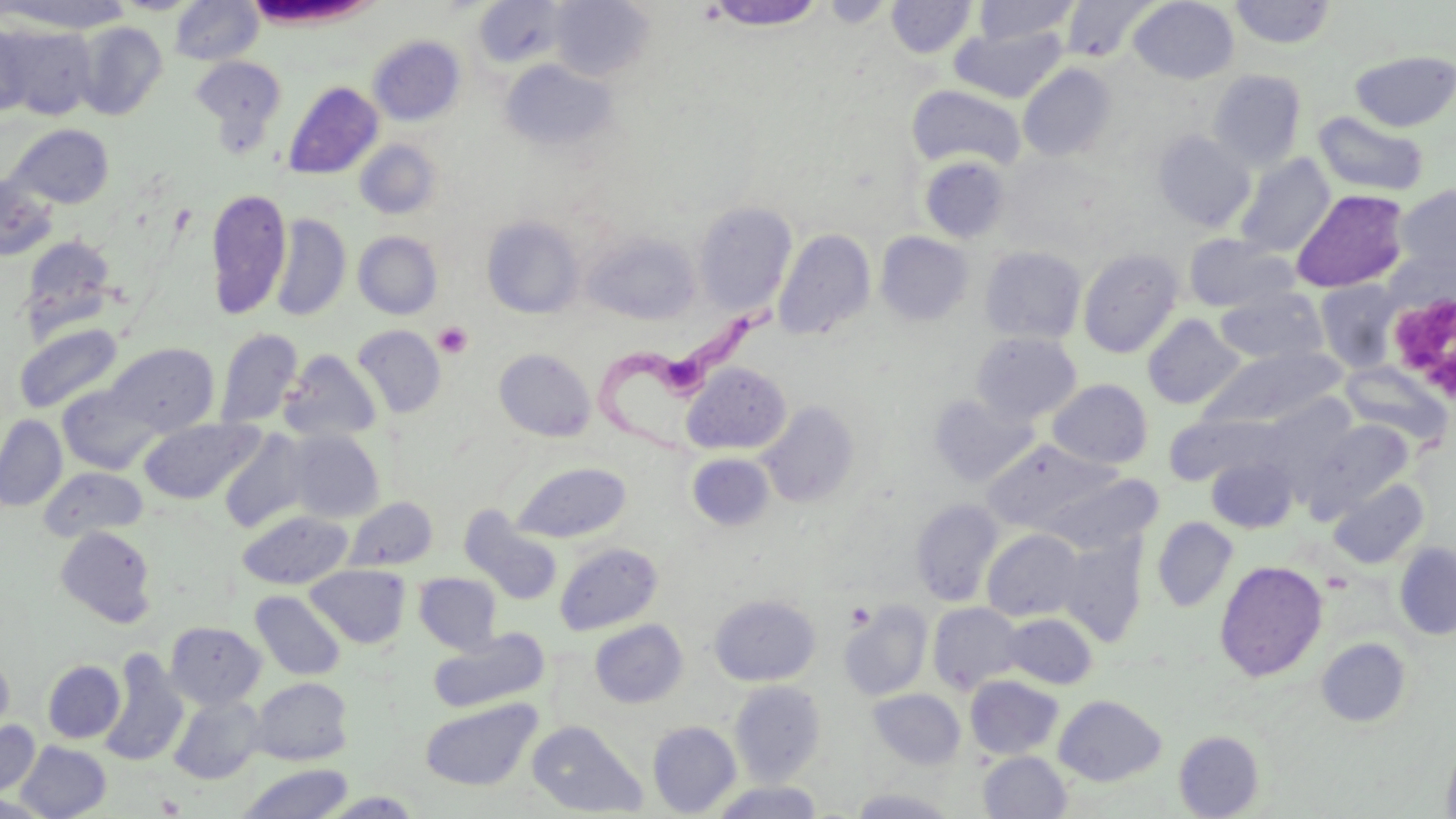

Approximate bounding boxes as named x1/y1/x2/y2 corners in pixels. Platelet locations: (x1=1386, y1=285, x2=1455, y2=409), (x1=434, y1=321, x2=473, y2=359), (x1=156, y1=794, x2=185, y2=816). Trypanosoma brucei locations: (x1=593, y1=297, x2=779, y2=458). Uninfected red blood cell locations: (x1=1, y1=0, x2=133, y2=33), (x1=170, y1=0, x2=263, y2=65), (x1=549, y1=0, x2=655, y2=82), (x1=886, y1=0, x2=977, y2=58), (x1=973, y1=0, x2=1079, y2=45), (x1=1129, y1=0, x2=1239, y2=84), (x1=472, y1=1, x2=568, y2=70), (x1=703, y1=1, x2=828, y2=31), (x1=1059, y1=1, x2=1154, y2=62), (x1=1229, y1=1, x2=1337, y2=49), (x1=73, y1=21, x2=168, y2=121), (x1=0, y1=23, x2=32, y2=117), (x1=2, y1=24, x2=97, y2=120), (x1=951, y1=26, x2=1067, y2=103), (x1=368, y1=36, x2=465, y2=125), (x1=1350, y1=50, x2=1456, y2=132), (x1=191, y1=56, x2=285, y2=140), (x1=500, y1=59, x2=617, y2=152), (x1=1018, y1=63, x2=1118, y2=162), (x1=1207, y1=69, x2=1306, y2=170), (x1=282, y1=81, x2=383, y2=180), (x1=907, y1=85, x2=1025, y2=171), (x1=1312, y1=111, x2=1429, y2=197), (x1=7, y1=123, x2=114, y2=209), (x1=1154, y1=130, x2=1255, y2=232), (x1=354, y1=139, x2=442, y2=219), (x1=1235, y1=153, x2=1334, y2=257), (x1=919, y1=155, x2=1011, y2=243), (x1=0, y1=173, x2=59, y2=263), (x1=1396, y1=185, x2=1456, y2=279), (x1=205, y1=188, x2=291, y2=320), (x1=1290, y1=188, x2=1409, y2=293), (x1=693, y1=201, x2=797, y2=315), (x1=271, y1=214, x2=351, y2=322), (x1=481, y1=216, x2=584, y2=319), (x1=773, y1=228, x2=876, y2=341), (x1=353, y1=231, x2=443, y2=320), (x1=582, y1=232, x2=699, y2=324), (x1=875, y1=232, x2=973, y2=325), (x1=1183, y1=234, x2=1300, y2=313), (x1=19, y1=235, x2=117, y2=336), (x1=980, y1=245, x2=1087, y2=345), (x1=1077, y1=248, x2=1184, y2=358), (x1=1314, y1=280, x2=1402, y2=372), (x1=1215, y1=288, x2=1328, y2=365), (x1=1142, y1=314, x2=1244, y2=409), (x1=14, y1=322, x2=123, y2=414), (x1=352, y1=324, x2=447, y2=419), (x1=215, y1=327, x2=303, y2=429), (x1=971, y1=332, x2=1082, y2=424), (x1=105, y1=342, x2=220, y2=434), (x1=1197, y1=346, x2=1345, y2=430), (x1=494, y1=348, x2=596, y2=441), (x1=279, y1=350, x2=383, y2=443), (x1=1340, y1=361, x2=1451, y2=448), (x1=682, y1=362, x2=791, y2=454), (x1=1048, y1=379, x2=1152, y2=468), (x1=58, y1=383, x2=163, y2=475), (x1=929, y1=394, x2=1037, y2=487), (x1=759, y1=400, x2=861, y2=508), (x1=1166, y1=413, x2=1277, y2=485), (x1=0, y1=415, x2=67, y2=511), (x1=138, y1=418, x2=263, y2=504), (x1=1308, y1=418, x2=1413, y2=514), (x1=219, y1=429, x2=313, y2=533), (x1=285, y1=430, x2=385, y2=522), (x1=984, y1=439, x2=1117, y2=532), (x1=687, y1=453, x2=775, y2=531), (x1=1206, y1=455, x2=1298, y2=533), (x1=511, y1=462, x2=632, y2=543), (x1=39, y1=467, x2=147, y2=542), (x1=1329, y1=479, x2=1428, y2=569), (x1=344, y1=497, x2=438, y2=572), (x1=910, y1=498, x2=1004, y2=607), (x1=462, y1=508, x2=562, y2=604), (x1=237, y1=510, x2=353, y2=589), (x1=1152, y1=517, x2=1238, y2=612), (x1=55, y1=525, x2=157, y2=627), (x1=982, y1=529, x2=1085, y2=623), (x1=1056, y1=532, x2=1148, y2=646), (x1=1394, y1=541, x2=1456, y2=640), (x1=555, y1=542, x2=662, y2=635), (x1=1214, y1=560, x2=1327, y2=681), (x1=305, y1=564, x2=410, y2=649), (x1=414, y1=573, x2=502, y2=654), (x1=251, y1=591, x2=346, y2=681), (x1=709, y1=594, x2=820, y2=686), (x1=839, y1=601, x2=932, y2=701), (x1=927, y1=602, x2=1024, y2=694), (x1=1000, y1=613, x2=1098, y2=689), (x1=590, y1=620, x2=688, y2=708), (x1=165, y1=621, x2=265, y2=709), (x1=429, y1=629, x2=550, y2=712), (x1=1316, y1=638, x2=1410, y2=727), (x1=99, y1=652, x2=189, y2=766), (x1=0, y1=654, x2=14, y2=740), (x1=42, y1=660, x2=125, y2=743), (x1=966, y1=675, x2=1063, y2=759), (x1=251, y1=677, x2=352, y2=765), (x1=730, y1=681, x2=826, y2=783), (x1=868, y1=688, x2=966, y2=769), (x1=1053, y1=694, x2=1166, y2=786), (x1=169, y1=695, x2=266, y2=784), (x1=420, y1=698, x2=541, y2=791), (x1=0, y1=720, x2=40, y2=797), (x1=527, y1=720, x2=647, y2=817), (x1=648, y1=721, x2=741, y2=816), (x1=1174, y1=730, x2=1264, y2=818), (x1=1441, y1=733, x2=1456, y2=819), (x1=15, y1=741, x2=111, y2=818), (x1=978, y1=750, x2=1071, y2=818), (x1=237, y1=763, x2=353, y2=819), (x1=709, y1=782, x2=825, y2=819), (x1=849, y1=788, x2=959, y2=818), (x1=322, y1=791, x2=424, y2=818), (x1=0, y1=794, x2=54, y2=817). Slide-level diagnosis: Trypanosoma brucei. One field of a larger specimen. Thin blood smear. Light microscopy. Image is 1456×819 pixels. May-Grünwald-Giemsa stain. 1000x magnification.